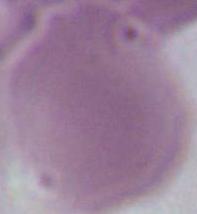
modality: micrograph
identification: red blood cell
magnification: 1000x